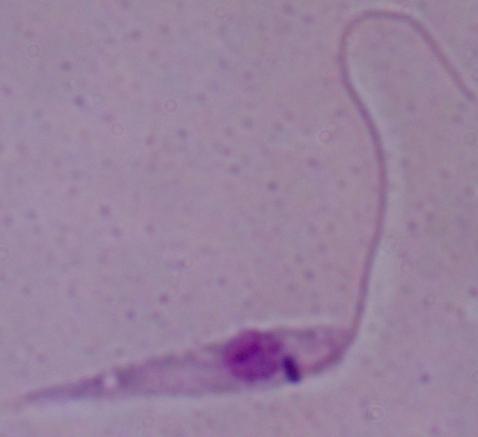 Micrograph. Captured at 1000x magnification. A Leishmania parasite is shown.